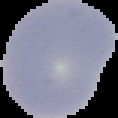

image type = segmented cell region on a black background
preparation = thin blood film
image size = 118×118 pixels
result = no Plasmodium parasites seen